Assess this cell for malaria.
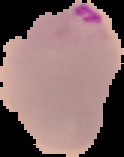
Parasitized.

Summary:
  - Preparation: thin blood film
  - Image size: 124×157 pixels
  - Image type: segmented cell region with the area outside set to black